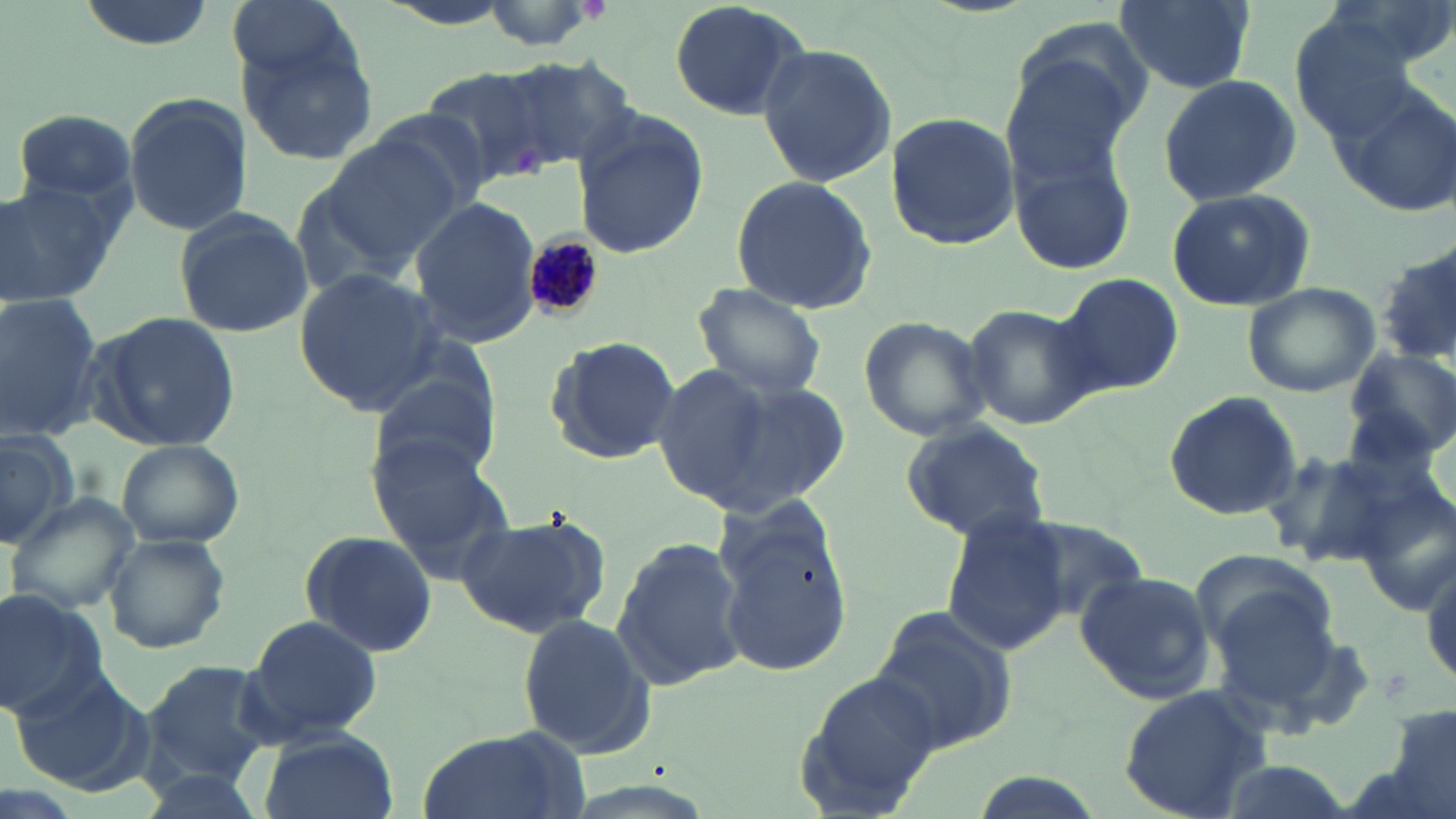
{
  "slide_level_diagnosis": "Plasmodium malariae",
  "field_of_view": "one of a larger specimen",
  "stain": "May-Grünwald-Giemsa",
  "image_size": "1456×819 pixels",
  "magnification": "1000x",
  "uninfected_red_blood_cell_locations": "approximate bounding boxes as (x1, y1, x2, y2) in pixels: (74, 0, 217, 49), (224, 0, 356, 87), (468, 0, 612, 53), (666, 0, 810, 122), (1115, 0, 1254, 92), (227, 24, 380, 165), (997, 32, 1147, 184), (756, 44, 898, 185), (493, 57, 634, 170), (421, 65, 562, 186), (1156, 73, 1303, 208), (1327, 84, 1456, 218), (121, 93, 252, 237), (11, 108, 141, 208), (571, 109, 709, 261), (884, 112, 1021, 251), (317, 136, 463, 266), (1005, 136, 1131, 275), (730, 173, 879, 316), (0, 177, 127, 312), (1164, 188, 1317, 313), (407, 197, 541, 348), (171, 206, 313, 339), (1375, 249, 1456, 365), (294, 267, 447, 415), (1053, 273, 1184, 395), (1242, 281, 1381, 397), (691, 283, 828, 404), (0, 295, 105, 439), (961, 302, 1095, 431), (86, 313, 241, 451), (855, 314, 993, 443), (542, 332, 682, 465), (1346, 345, 1456, 463), (648, 360, 837, 516), (373, 365, 505, 485), (1164, 390, 1302, 519), (899, 420, 1052, 543), (0, 424, 77, 542), (366, 432, 515, 571), (114, 437, 244, 550), (1261, 446, 1401, 566), (7, 493, 137, 618), (713, 498, 851, 675), (940, 510, 1073, 655), (457, 512, 609, 639), (1017, 519, 1150, 621), (301, 530, 440, 657), (105, 534, 230, 652), (609, 536, 745, 693), (1189, 550, 1340, 658), (1422, 553, 1455, 691), (1073, 570, 1215, 706), (0, 589, 108, 720), (1208, 590, 1344, 716), (870, 606, 1020, 754), (515, 612, 657, 758), (245, 615, 383, 742), (144, 659, 273, 785), (795, 667, 945, 815), (7, 669, 150, 791), (1116, 682, 1276, 817), (1382, 706, 1456, 819), (416, 728, 584, 819), (260, 732, 396, 819)",
  "preparation": "thin blood film",
  "plasmodium_malariae_infected_red_blood_cell_locations": "approximate bounding boxes as (x1, y1, x2, y2) in pixels: (519, 225, 613, 322)",
  "modality": "light microscopy"
}